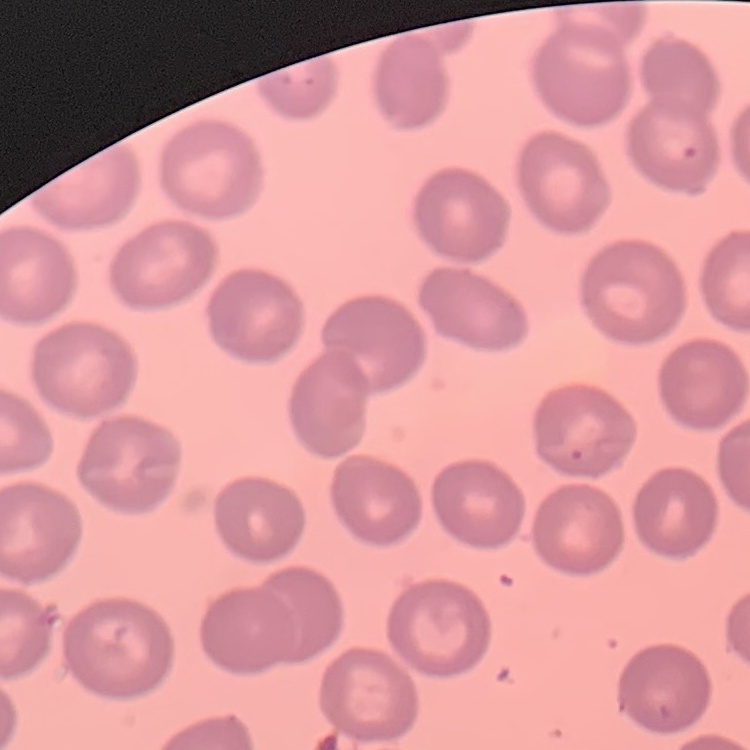
Summary:
  - Red blood cell morphology: no rouleaux formation
  - Stain: Field's or Giemsa
  - Image type: square crop of a larger photomicrograph
  - Preparation: thin blood smear